Give the position of every leukocyte visible.
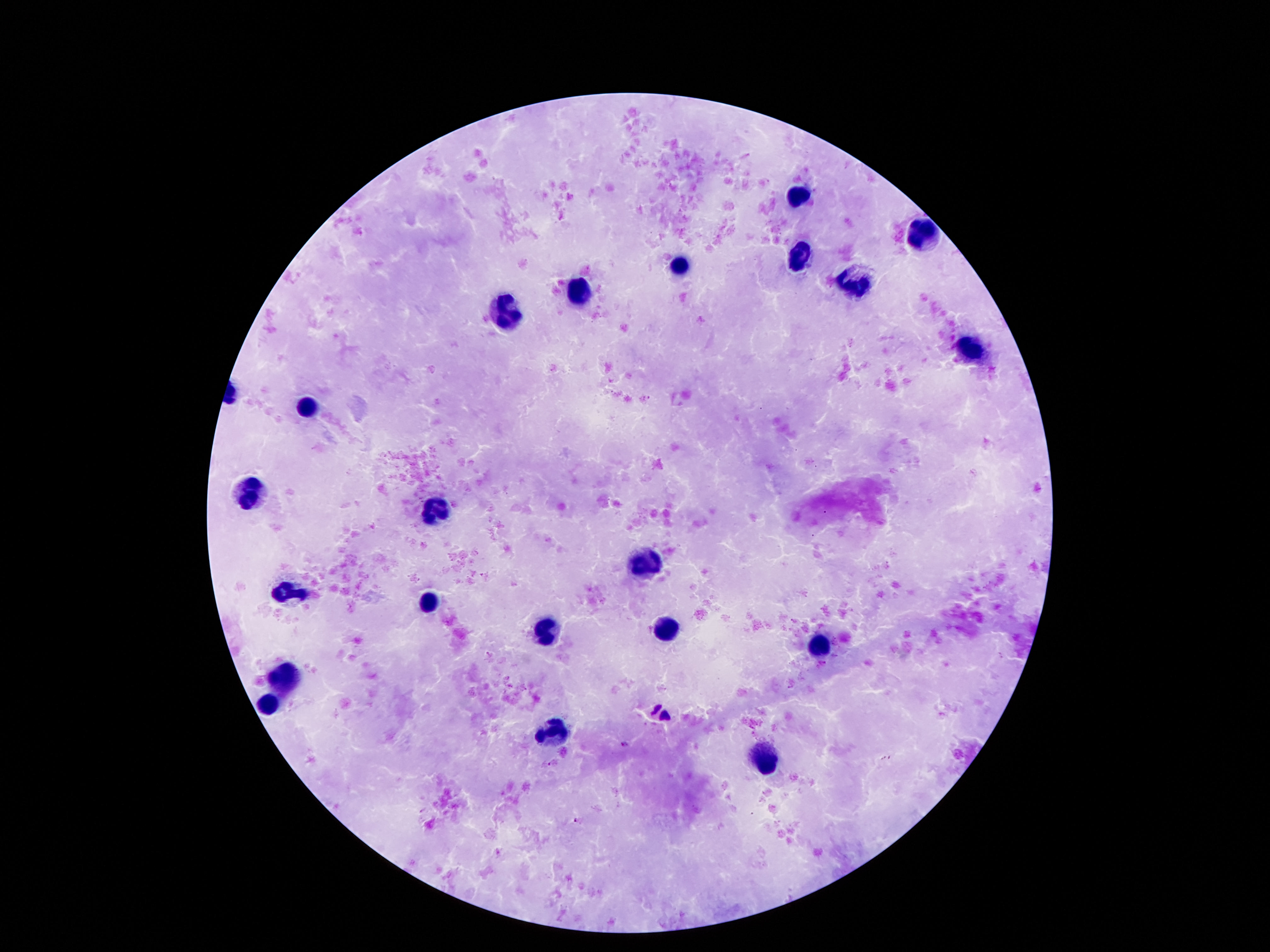
Approximate object centers, in pixels from the top-left corner.
Leukocytes: (x=796, y=196), (x=924, y=231), (x=802, y=259), (x=679, y=266), (x=856, y=284), (x=579, y=293), (x=506, y=317), (x=970, y=350), (x=307, y=404), (x=248, y=495), (x=435, y=508), (x=648, y=561), (x=285, y=586), (x=427, y=600), (x=546, y=629), (x=667, y=631), (x=816, y=647), (x=287, y=678), (x=270, y=702), (x=553, y=731), (x=763, y=757).

magnification = 100x
field of view = single
image size = 1270×952 pixels
patient malaria status = not infected
preparation = thick blood smear
stain = Giemsa
capture = smartphone camera through the microscope eyepiece